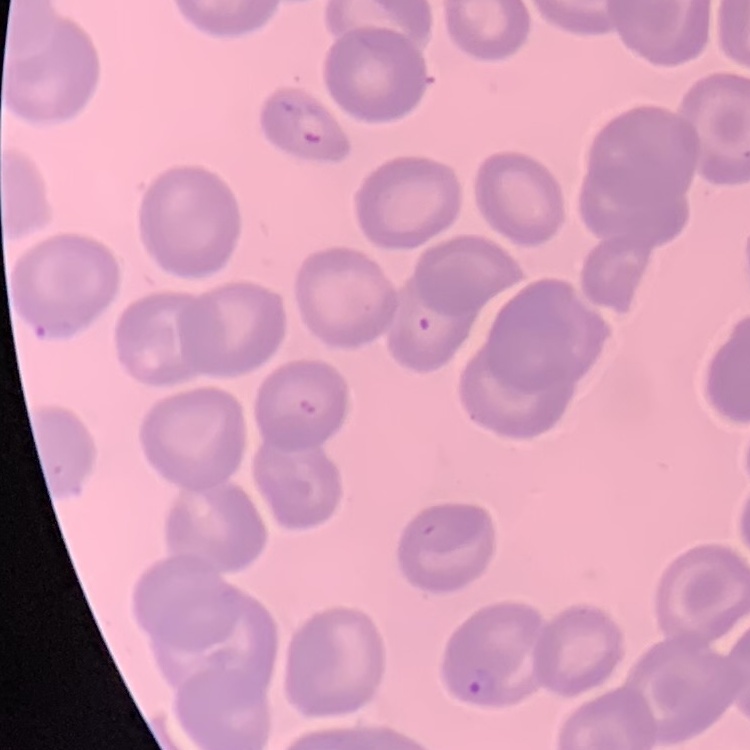

The red blood cells show no rouleaux formation. Stained with either Field's or Giemsa. Thin peripheral smear. Square crop of a larger photomicrograph.